Outline each Plasmodium falciparum-infected red blood cell.
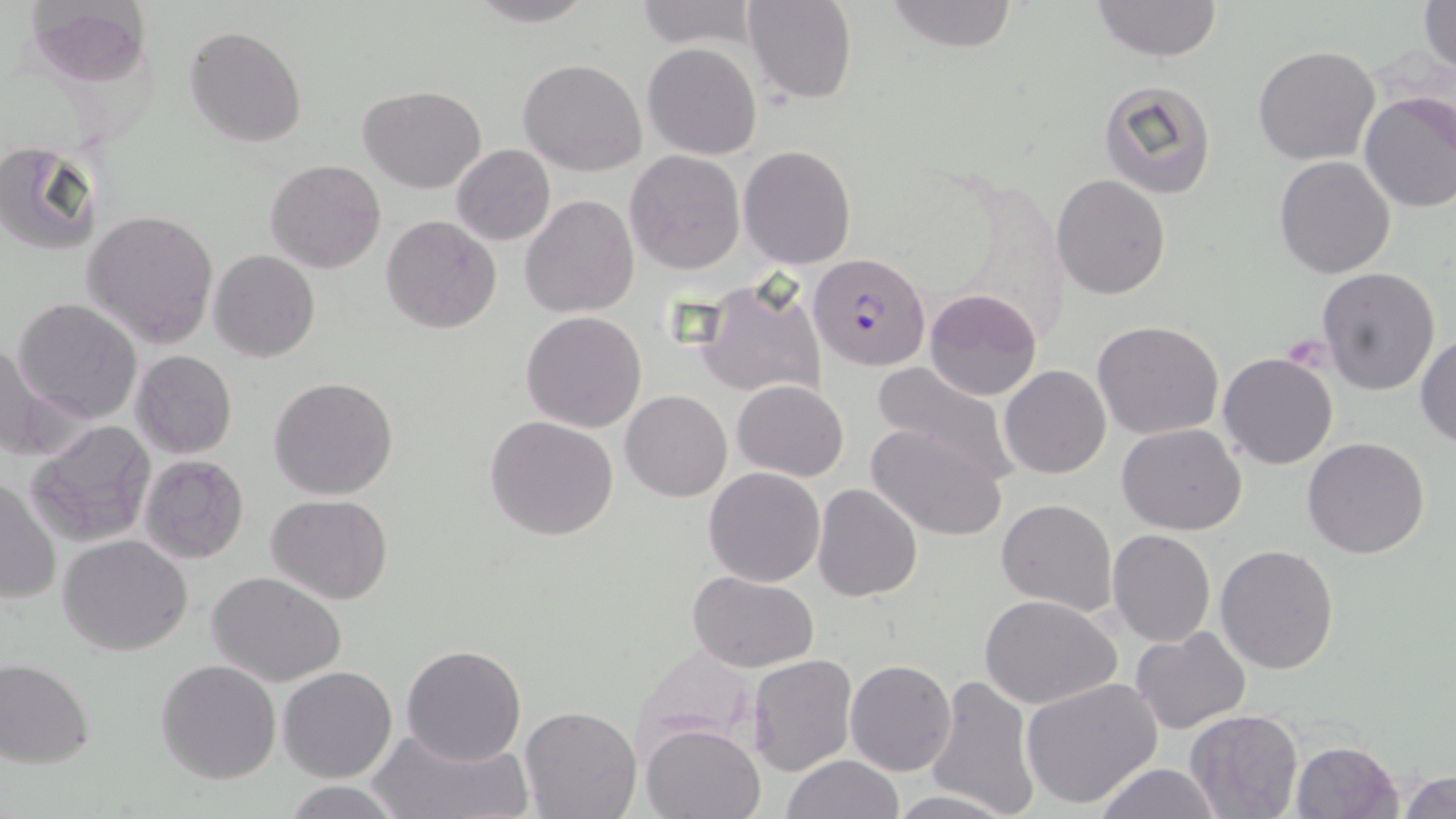

Approximate bounding boxes as (x1, y1, x2, y2) in pixels.
Plasmodium falciparum-infected red blood cells: (807, 252, 931, 371).

slide_level_diagnosis: Plasmodium falciparum
modality: optical microscopy
magnification: 1000x
image_size: 1456×819 pixels
stain: May-Grünwald-Giemsa
field_of_view: single
preparation: thin blood film
uninfected_red_blood_cell_locations: 'approximate bounding boxes as (x1, y1, x2, y2) in pixels: (23, 0, 150, 87), (461, 0, 598, 27), (744, 0, 856, 105), (885, 0, 1019, 53), (1092, 0, 1222, 62), (633, 1, 759, 50), (1418, 1, 1455, 72), (186, 25, 307, 148), (642, 42, 762, 161), (1252, 45, 1380, 165), (518, 58, 647, 176), (1096, 79, 1217, 199), (358, 84, 486, 194), (1359, 92, 1456, 212), (0, 142, 102, 256), (451, 144, 556, 246), (738, 144, 856, 267), (625, 150, 746, 275), (1274, 155, 1396, 278), (264, 159, 386, 274), (1051, 173, 1172, 299), (519, 193, 638, 318), (82, 208, 221, 347), (381, 215, 501, 335), (209, 250, 320, 363), (1316, 266, 1441, 396), (692, 277, 828, 401), (924, 288, 1042, 402), (12, 298, 143, 424), (520, 310, 648, 433), (1092, 320, 1225, 439), (1415, 334, 1456, 446), (0, 338, 64, 463), (132, 351, 237, 459), (1218, 352, 1339, 471), (871, 361, 1019, 479), (1000, 366, 1111, 479), (269, 377, 400, 500), (733, 380, 849, 480), (620, 390, 732, 502), (485, 414, 618, 540), (25, 419, 157, 546), (866, 421, 1007, 540), (1117, 423, 1247, 534), (1303, 436, 1431, 558), (139, 454, 249, 563), (703, 466, 826, 586), (1, 477, 61, 605), (813, 483, 924, 602), (267, 494, 394, 606), (996, 498, 1118, 615), (1107, 529, 1216, 647), (58, 534, 192, 656), (1214, 544, 1340, 674), (207, 571, 347, 686), (688, 573, 819, 671), (981, 594, 1123, 709), (1132, 625, 1250, 733), (632, 643, 761, 754), (402, 645, 527, 765), (749, 653, 858, 777), (282, 657, 530, 777), (0, 658, 96, 769), (155, 659, 282, 785), (846, 659, 956, 777), (279, 666, 397, 782), (925, 674, 1041, 819), (1021, 677, 1165, 811), (518, 706, 641, 819), (1186, 708, 1304, 818), (641, 722, 766, 818), (370, 724, 531, 819), (1288, 740, 1404, 819), (782, 754, 905, 818), (1092, 762, 1227, 819), (1398, 769, 1456, 819), (281, 779, 412, 818), (885, 790, 1019, 819)'